Report the malaria status of this cell.
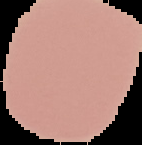
It is uninfected.

preparation = thin blood smear
image type = segmented cell region with the area outside set to black
image size = 142×145 pixels